Comment on the morphology of the red blood cells.
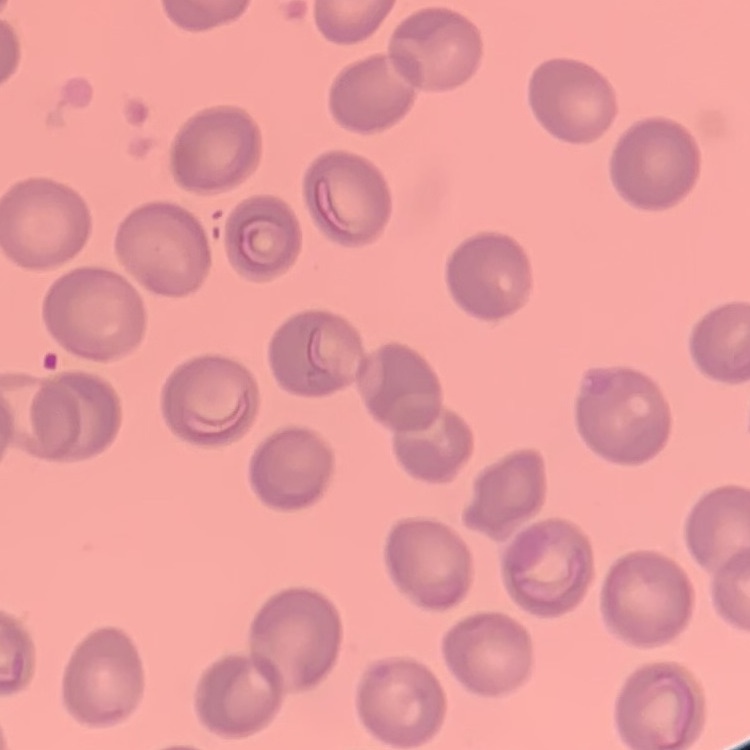

No rouleaux formation.

Stained with either Field's or Giemsa. One tile cut from a larger photomicrograph. Thin peripheral smear.